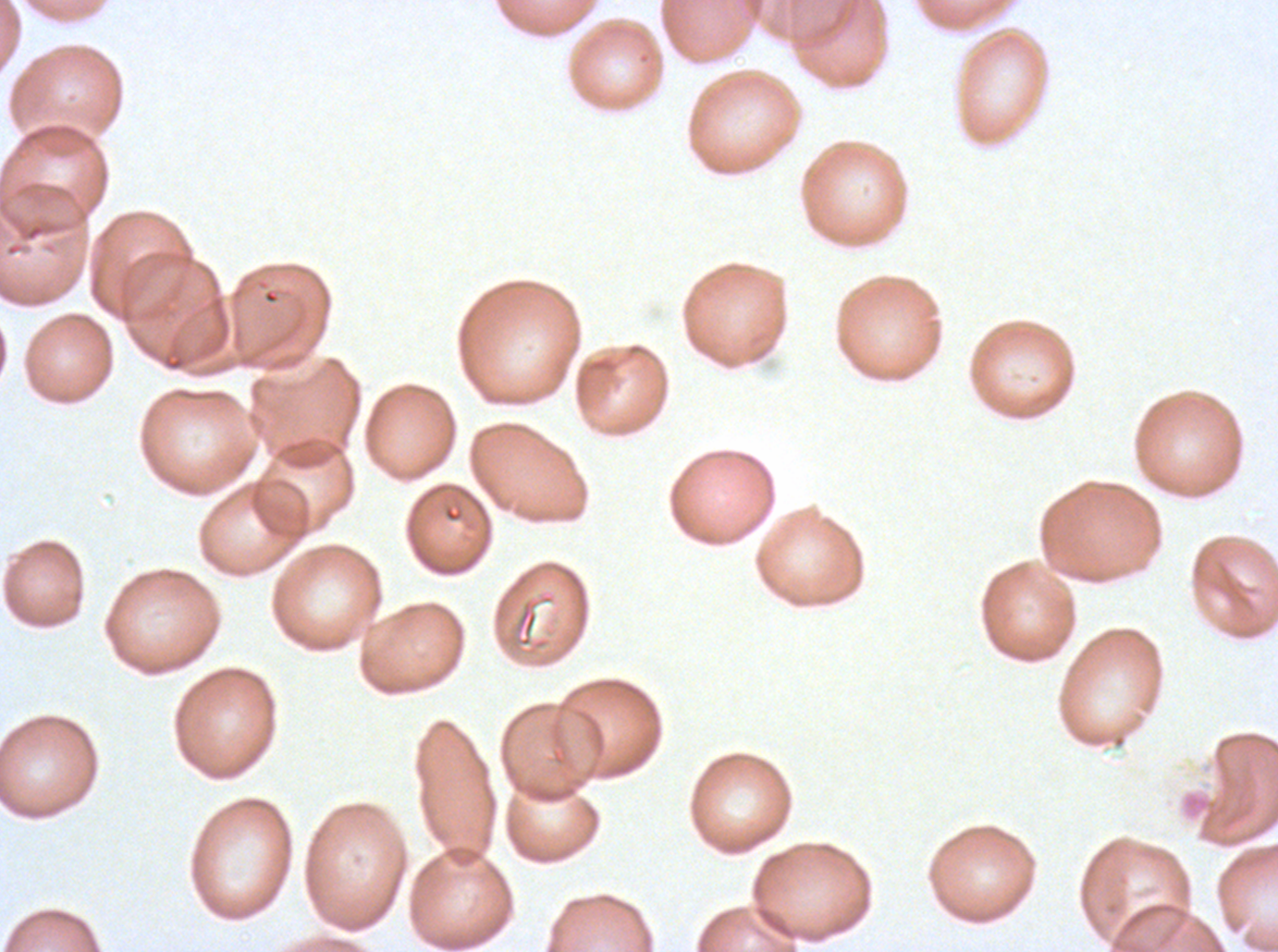

notation = approximate bounding boxes as [x1, y1, x2, y2] in pixels
debris locations = [515, 599, 538, 648]
field of view = sub-image separated from a larger composite
specimen = P. falciparum cultured ex vivo for 24 to 48 hours, from a patient in The Gambia
preparation = thin blood smear
stain = Giemsa
image size = 1278×952 pixels